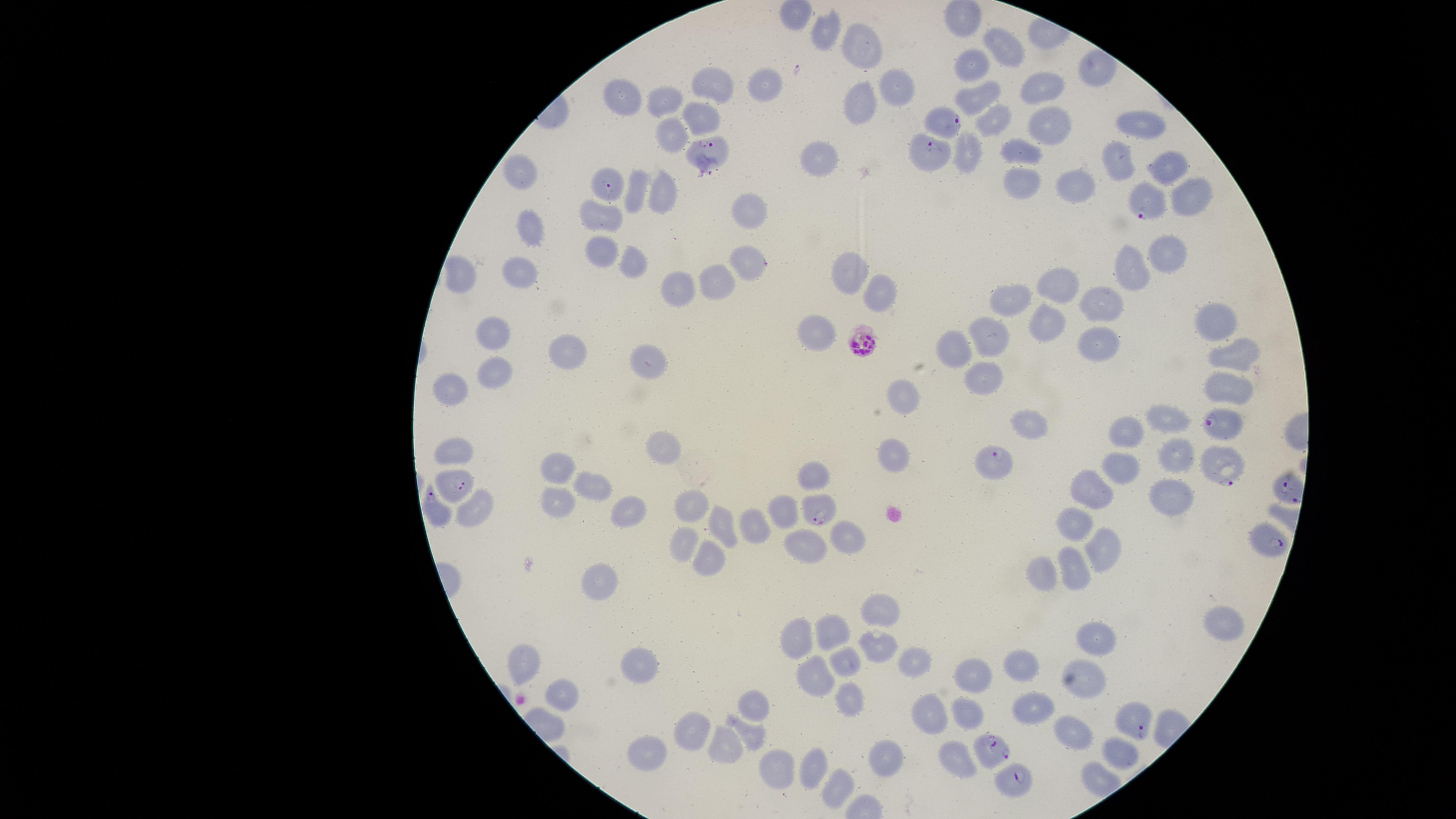

Approximate marker points as [x, y] in pixels. Uninfected RBCs: [826, 30], [1001, 46], [855, 54], [967, 70], [766, 83], [724, 88], [1041, 91], [621, 94], [891, 94], [980, 94], [855, 104], [676, 105], [701, 115], [989, 122], [1148, 123], [1045, 126], [673, 138], [1020, 148], [965, 151], [823, 155], [1117, 159], [1160, 162], [526, 171], [1016, 177], [1077, 186], [637, 191], [663, 191], [1186, 195], [748, 209], [603, 217], [532, 230], [1163, 248], [604, 249], [623, 259], [845, 268], [522, 270], [1133, 271], [462, 276], [713, 282], [676, 286], [876, 287], [1065, 288], [1017, 302], [1107, 302], [1049, 319], [1218, 319], [814, 327], [997, 336], [486, 340], [1100, 342], [962, 343], [1238, 353], [573, 357], [645, 366], [499, 375], [990, 375], [1230, 379], [454, 389], [900, 398], [1030, 423], [1169, 423], [1124, 437], [456, 451], [891, 451], [664, 456], [1181, 460], [560, 462], [816, 468], [1124, 470], [587, 482], [1092, 490], [1164, 493], [555, 503], [690, 508], [634, 511], [473, 512], [777, 514], [723, 522], [1076, 522], [754, 530], [849, 536], [1107, 544], [673, 548], [797, 549], [702, 559], [1074, 562], [1042, 572], [604, 588], [886, 611], [1221, 622], [830, 633], [1095, 638], [795, 643], [874, 644], [528, 659], [840, 660], [917, 662], [1021, 667], [639, 671], [812, 674], [1089, 674], [970, 678], [564, 689], [851, 700], [754, 702], [1033, 708], [964, 710], [930, 715], [1078, 730], [694, 732], [751, 734], [721, 743], [1118, 751], [886, 752], [644, 757], [955, 757], [808, 770], [772, 775], [837, 787]. Parasitized RBCs: [942, 119], [712, 145], [929, 156], [604, 182], [1150, 203], [747, 259], [863, 342], [1228, 427], [998, 461], [1219, 465], [454, 484], [1283, 489], [434, 505], [824, 512], [1270, 543], [1134, 723], [993, 750], [1016, 782]. Presence: malaria parasites seen. Species: Plasmodium falciparum. Single field of view. Giemsa-stained preparation. Thin blood smear. Image is 1456×819 pixels. The visible region is circular. Smartphone photograph through the microscope eyepiece.